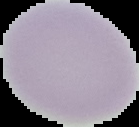

Summary:
  - Preparation: thin blood film
  - Image size: 139×127 pixels
  - Image type: segmented cell region on a black background
  - Malaria status: uninfected